Report the malaria status of this cell.
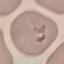

It is parasitized.

stain = Giemsa
capture = smartphone through the microscope eyepiece
image type = cell patch, automatically extracted from a larger field of view and resized to 64 × 64 pixels
preparation = thin blood smear